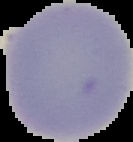
{
  "image_type": "cell region segmented out of the field of view; surrounding area masked to black",
  "preparation": "thin blood film",
  "malaria_status": "uninfected",
  "image_size": "133×142 pixels"
}